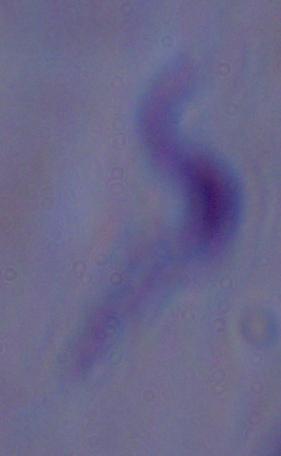

Summary:
  - Modality: photomicrograph
  - Identification: trypanosome
  - Magnification: 1000x